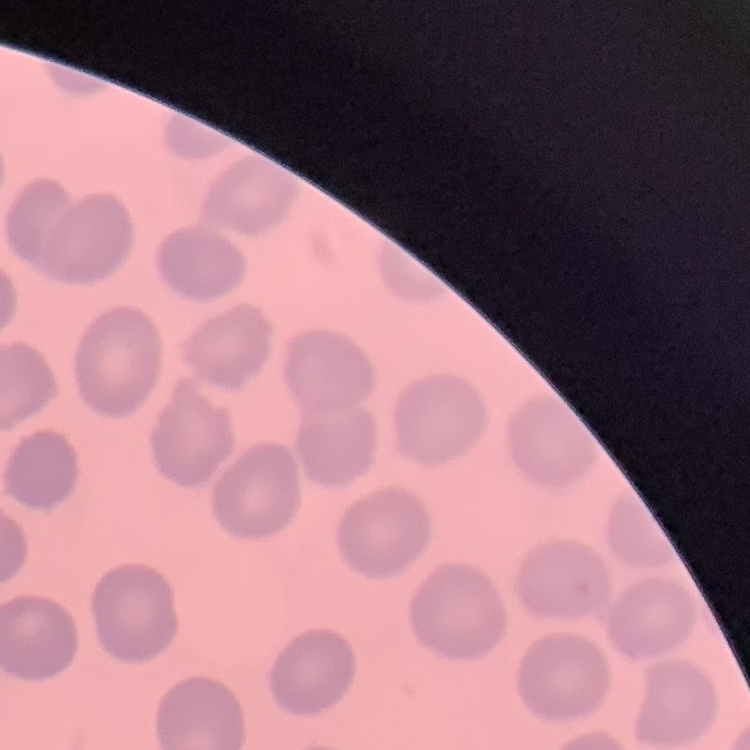

Summary:
  - Erythrocyte morphology: no rouleaux formation
  - Stain: Field's or Giemsa
  - Preparation: thin peripheral smear
  - Image type: square crop of a larger photomicrograph